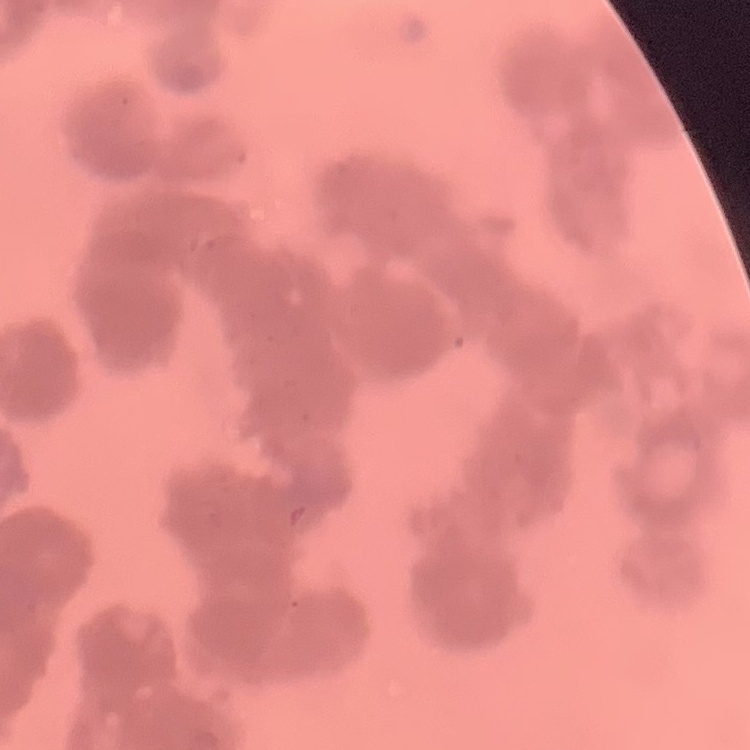
The erythrocytes show rouleaux formation. Stained with either Field's or Giemsa. Thin peripheral smear. Square crop of a larger photomicrograph.